Assess this cell for malaria.
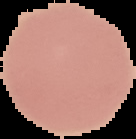

It is uninfected.

Summary:
  - Preparation: thin blood smear
  - Image type: segmented cell region on a black background
  - Image size: 136×139 pixels